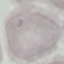
Result: no malaria parasites seen. Photographed with a smartphone camera at the microscope eyepiece. Cell patch, automatically extracted from a larger field of view and resized to 64 × 64 pixels. Giemsa-stained preparation. Thin smear of blood.